Describe the morphology of the red blood cells.
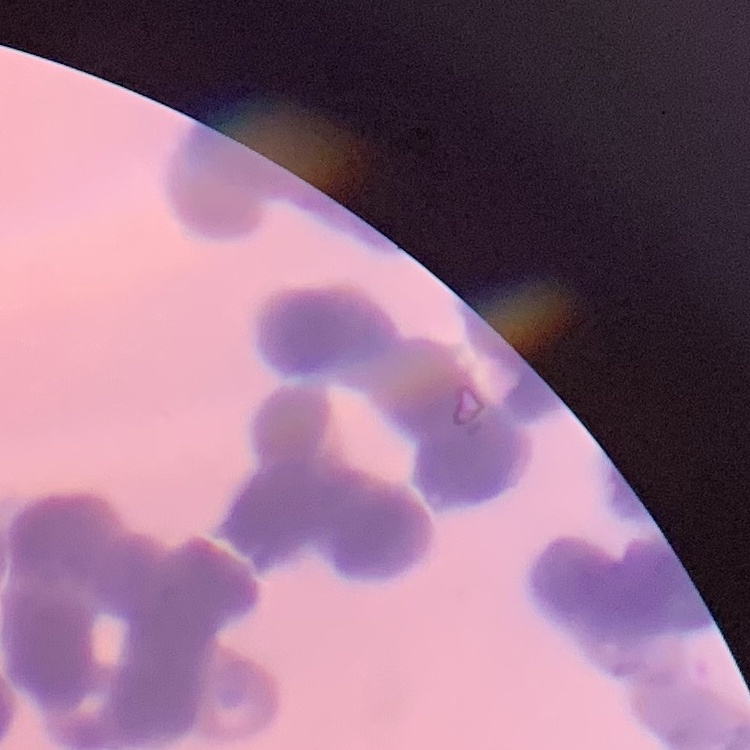
Rouleaux formation.

preparation = thin blood smear
image type = one tile cut from a larger photomicrograph
stain = Field's or Giemsa